Locate every Plasmodium ovale-infected red blood cell.
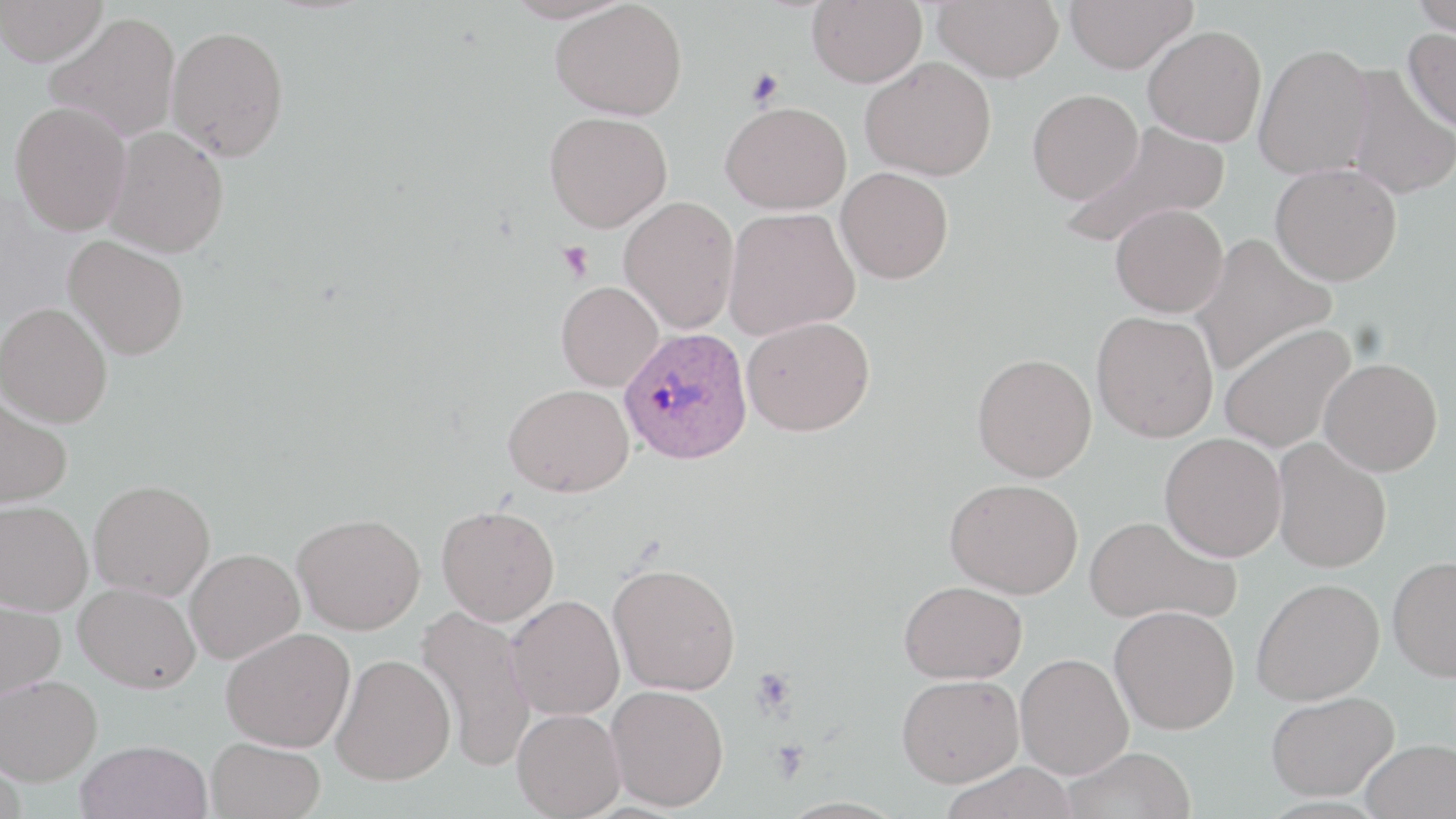
Approximate bounding boxes as (x1, y1, x2, y2) in pixels.
Plasmodium ovale-infected red blood cells: (619, 327, 752, 464).

{
  "slide_level_diagnosis": "Plasmodium ovale",
  "platelet_locations": "approximate bounding boxes as (x1, y1, x2, y2) in pixels: (745, 67, 785, 109), (558, 241, 594, 282), (750, 668, 796, 717), (770, 739, 808, 782)",
  "magnification": "1000x",
  "field_of_view": "single",
  "uninfected_red_blood_cell_locations": "approximate bounding boxes as (x1, y1, x2, y2) in pixels: (0, 0, 107, 66), (503, 0, 635, 24), (807, 0, 927, 88), (932, 0, 1064, 82), (1064, 0, 1198, 73), (1411, 0, 1455, 40), (550, 1, 687, 120), (45, 12, 181, 142), (165, 25, 289, 161), (1143, 25, 1267, 147), (1403, 27, 1456, 133), (1254, 43, 1374, 180), (860, 57, 996, 180), (1343, 63, 1456, 201), (1027, 89, 1143, 204), (9, 100, 132, 236), (721, 101, 852, 214), (544, 111, 673, 232), (1062, 122, 1229, 251), (104, 126, 229, 258), (1270, 163, 1402, 286), (835, 167, 954, 284), (619, 196, 740, 334), (1111, 204, 1228, 317), (723, 207, 861, 339), (1189, 233, 1336, 376), (63, 236, 190, 360), (556, 281, 664, 391), (0, 302, 113, 427), (1091, 310, 1219, 442), (741, 316, 875, 436), (1219, 323, 1356, 454), (972, 353, 1097, 481), (1319, 357, 1443, 476), (503, 384, 634, 497), (0, 392, 73, 509), (1160, 432, 1287, 561), (1272, 438, 1392, 573), (945, 478, 1084, 598), (89, 479, 215, 601), (1, 500, 93, 616), (436, 504, 560, 625), (292, 513, 425, 634), (1084, 515, 1240, 627), (184, 548, 305, 663), (1387, 555, 1456, 682), (608, 562, 741, 696), (1251, 578, 1384, 705), (899, 580, 1027, 683), (74, 582, 200, 692), (506, 594, 625, 720), (0, 597, 66, 704), (1109, 605, 1240, 734), (416, 607, 536, 773), (222, 627, 355, 752), (331, 652, 456, 785), (1016, 653, 1133, 778), (0, 674, 102, 785), (897, 674, 1024, 786), (605, 685, 728, 811), (1266, 691, 1398, 800), (512, 708, 626, 818), (206, 737, 326, 819), (1361, 739, 1455, 819), (76, 740, 213, 819), (1062, 747, 1196, 819), (939, 761, 1080, 819)",
  "modality": "optical microscopy",
  "image_size": "1456×819 pixels",
  "preparation": "thin blood smear",
  "stain": "May-Grünwald-Giemsa"
}